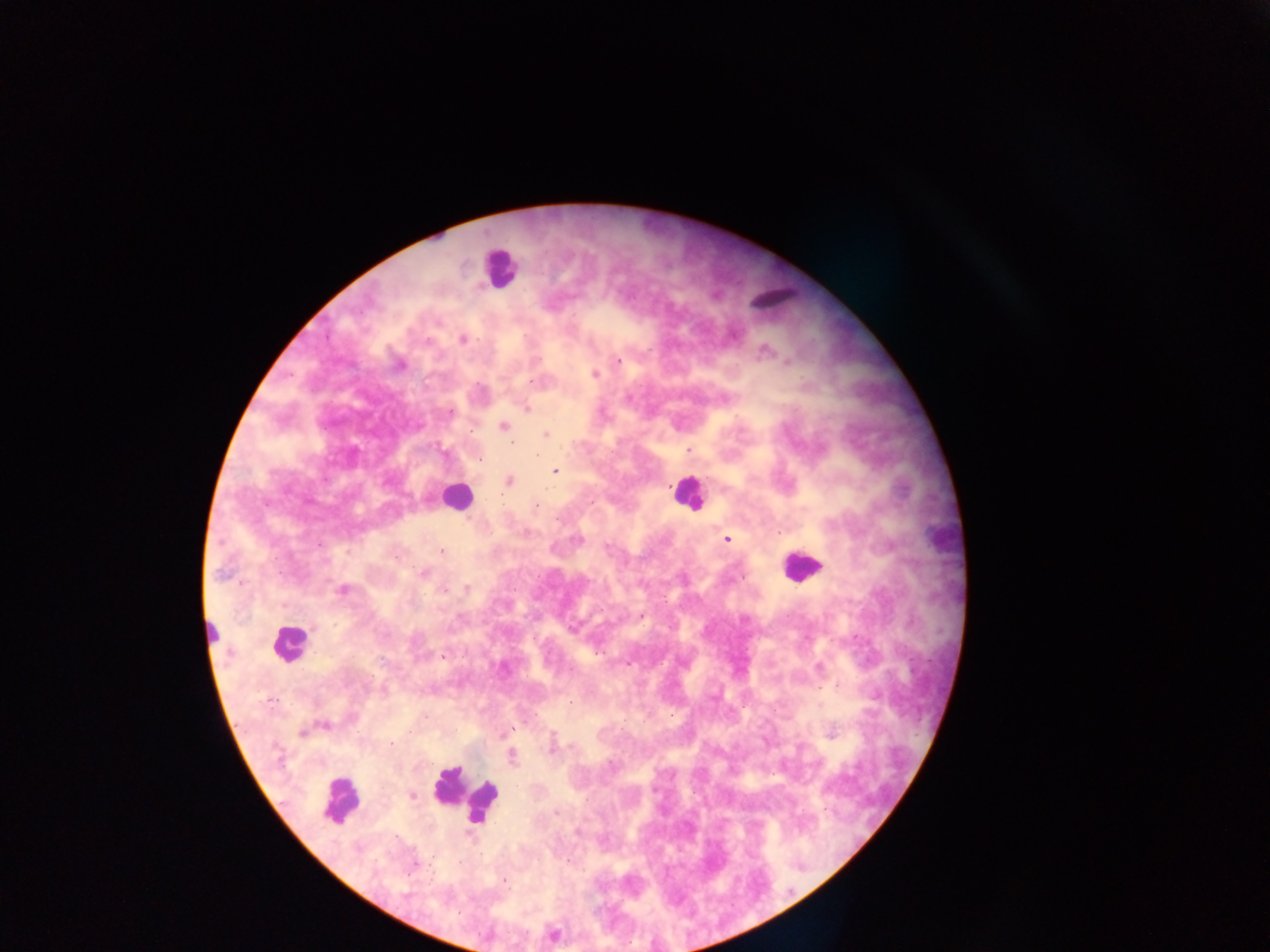
{
  "country": "Ghana",
  "preparation": "thick blood smear",
  "field_of_view": "single",
  "image_size": "1270×952 pixels",
  "capture": "mobile-phone photograph through a microscope",
  "plasmodium_parasite_locations": "approximate centers as [x, y] in pixels: [715, 297], [765, 349], [535, 357], [619, 359], [788, 361], [594, 374], [527, 408], [449, 413], [503, 425], [544, 434], [513, 442], [689, 449], [536, 457], [556, 470], [510, 481], [535, 505], [727, 539], [440, 552], [424, 573], [466, 589], [341, 590], [575, 625], [595, 651], [444, 655], [821, 707], [325, 725], [832, 732], [301, 734], [502, 734], [392, 743], [574, 749], [512, 758], [412, 797], [558, 812], [504, 880]",
  "leukocyte_locations": "approximate centers as [x, y] in pixels: [493, 270], [454, 496], [690, 496], [798, 566], [291, 645], [466, 797], [342, 798]"
}